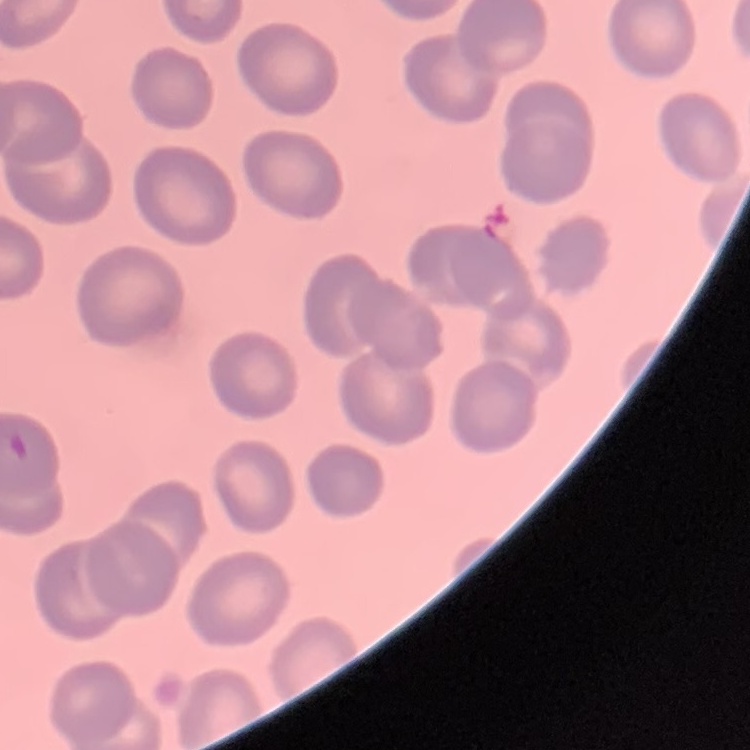

erythrocyte morphology = no rouleaux formation
stain = Field's or Giemsa
preparation = thin blood film
image type = one tile cut from a larger photomicrograph